Classify this cell by malaria status.
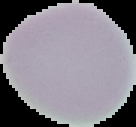

Uninfected.

Image is 136×127 pixels. From a thin blood smear. Segmented cell region on a black background.